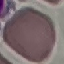
Malaria status: uninfected. Giemsa stain. Photographed with a smartphone camera at the microscope eyepiece. Thin smear of blood. Automatically extracted cell patch, resized to 64 × 64 pixels.